Draw a bounding box around every leukocyte (white blood cell).
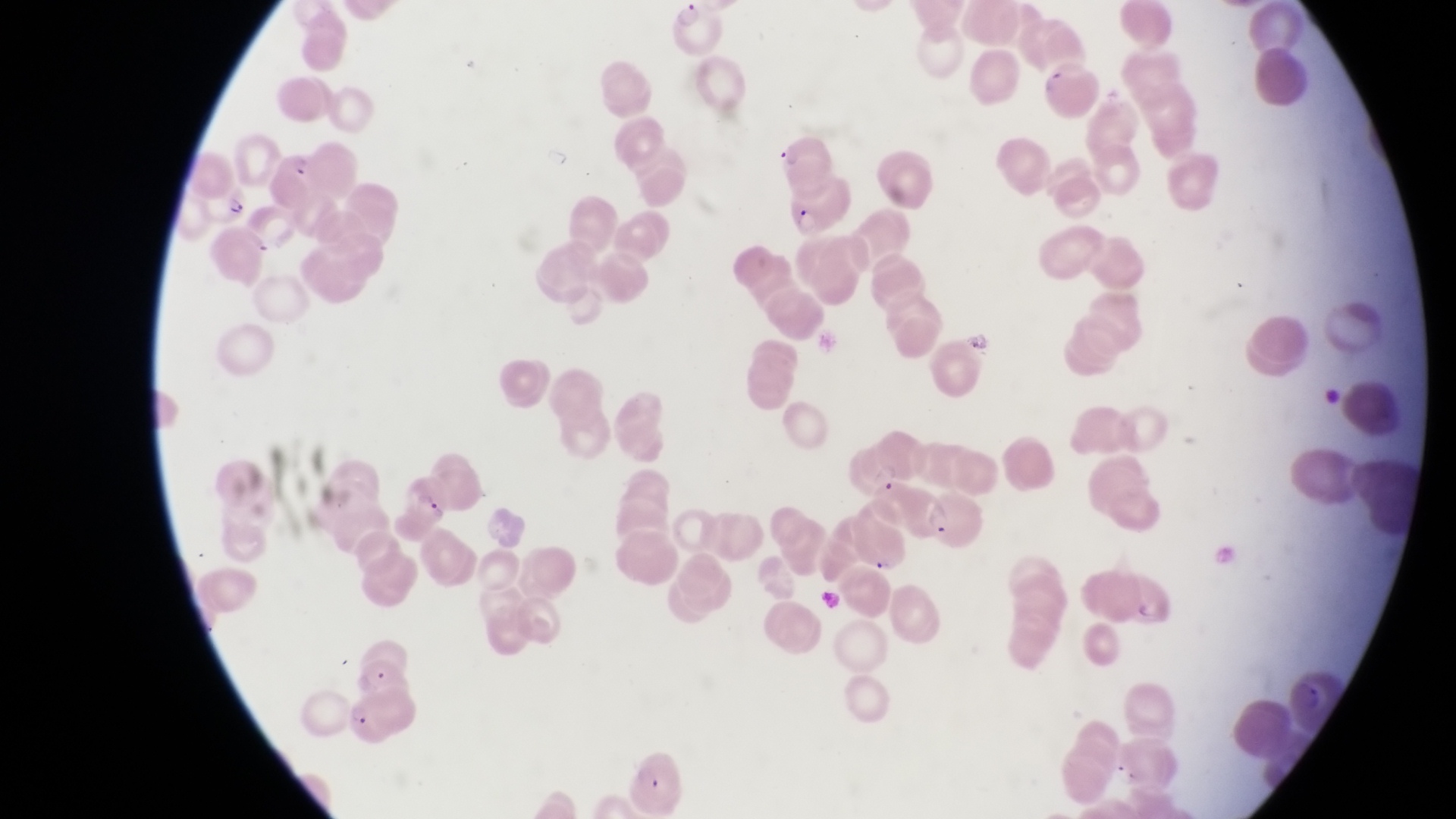

No leukocytes observed.

Approximate bounding boxes as left top right bottom in pixels.
Summary:
  - Parasitised red blood cell locations: 278 148 337 211; 219 182 255 228; 785 184 858 237; 842 444 906 494; 396 468 454 527; 353 652 414 698; 350 704 413 746; 629 743 689 816
  - Trophozoite locations: 965 322 994 361
  - Field of view: single
  - Image size: 1456×819 pixels
  - Magnification: 1000x
  - Preparation: thin blood smear
  - Capture: smartphone photograph through the eyepiece of an Olympus CX-23 microscope
  - Country: Uganda